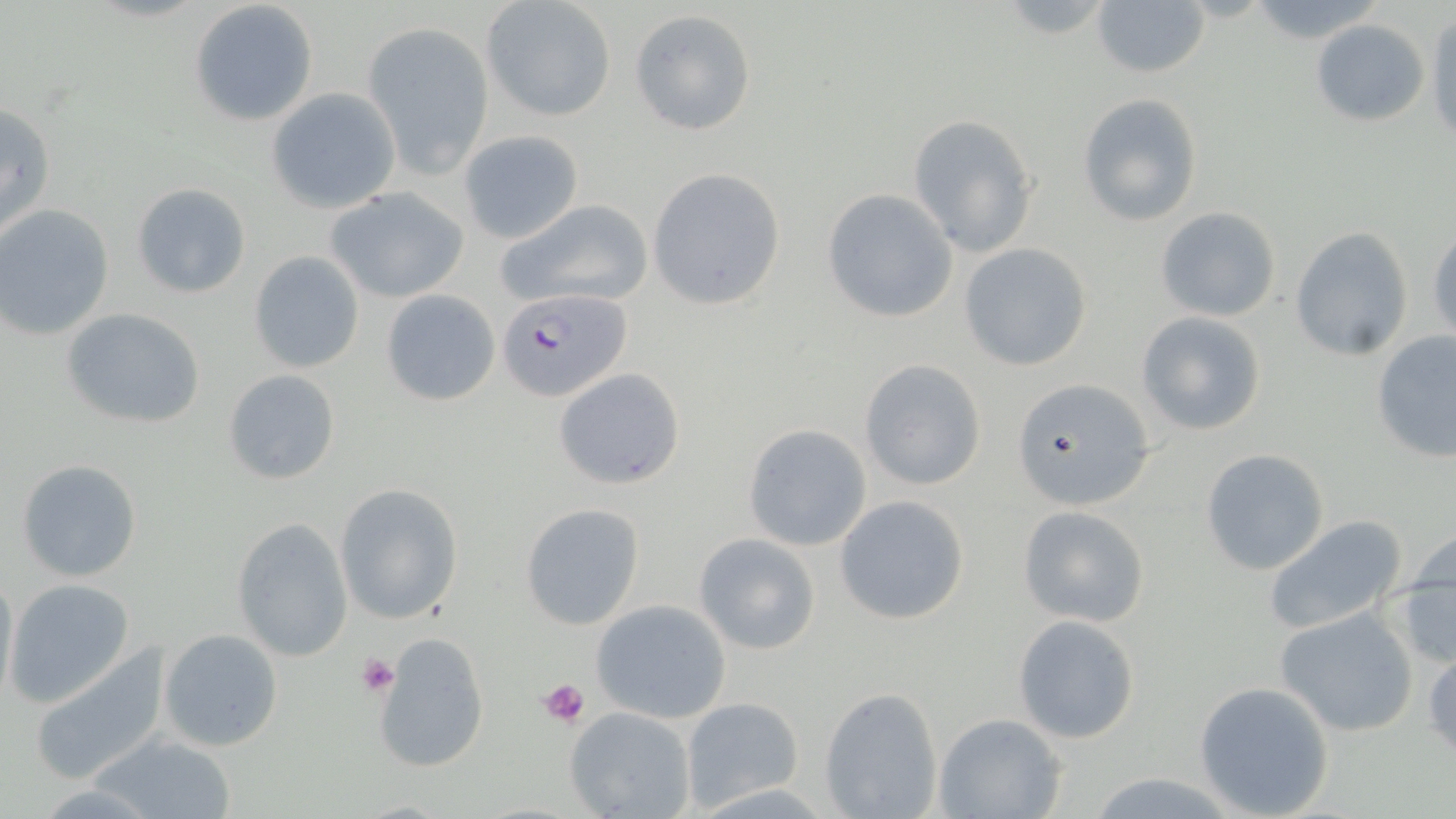

Summary:
  - Coordinate format: approximate bounding boxes as named x1/y1/x2/y2 corners in pixels
  - Platelet locations: (x1=356, y1=654, x2=400, y2=696), (x1=538, y1=676, x2=592, y2=728)
  - Plasmodium falciparum-infected red blood cell locations: (x1=498, y1=289, x2=631, y2=402)
  - Uninfected red blood cell locations: (x1=482, y1=0, x2=616, y2=121), (x1=190, y1=1, x2=317, y2=125), (x1=1092, y1=3, x2=1210, y2=79), (x1=629, y1=9, x2=757, y2=135), (x1=1425, y1=14, x2=1455, y2=150), (x1=1311, y1=18, x2=1429, y2=126), (x1=361, y1=21, x2=494, y2=175), (x1=267, y1=88, x2=401, y2=212), (x1=1077, y1=93, x2=1203, y2=225), (x1=1, y1=99, x2=56, y2=239), (x1=907, y1=114, x2=1039, y2=258), (x1=459, y1=129, x2=584, y2=243), (x1=647, y1=167, x2=786, y2=311), (x1=132, y1=182, x2=249, y2=298), (x1=324, y1=187, x2=469, y2=304), (x1=822, y1=188, x2=958, y2=322), (x1=497, y1=199, x2=654, y2=311), (x1=0, y1=203, x2=115, y2=340), (x1=1156, y1=206, x2=1280, y2=321), (x1=1427, y1=225, x2=1456, y2=343), (x1=1289, y1=226, x2=1414, y2=360), (x1=959, y1=243, x2=1092, y2=371), (x1=249, y1=250, x2=366, y2=372), (x1=379, y1=289, x2=501, y2=407), (x1=61, y1=307, x2=205, y2=428), (x1=1135, y1=310, x2=1268, y2=436), (x1=1371, y1=330, x2=1456, y2=464), (x1=860, y1=359, x2=987, y2=490), (x1=553, y1=367, x2=685, y2=490), (x1=222, y1=370, x2=342, y2=485), (x1=1014, y1=379, x2=1155, y2=509), (x1=742, y1=423, x2=873, y2=552), (x1=1199, y1=448, x2=1329, y2=576), (x1=15, y1=458, x2=143, y2=583), (x1=334, y1=484, x2=464, y2=625), (x1=834, y1=495, x2=970, y2=625), (x1=520, y1=502, x2=646, y2=628), (x1=1017, y1=505, x2=1149, y2=627), (x1=1261, y1=514, x2=1408, y2=637), (x1=230, y1=518, x2=352, y2=661), (x1=693, y1=532, x2=821, y2=654), (x1=1393, y1=539, x2=1456, y2=668), (x1=0, y1=568, x2=19, y2=706), (x1=4, y1=580, x2=134, y2=707), (x1=592, y1=600, x2=731, y2=722), (x1=1275, y1=607, x2=1421, y2=737), (x1=1014, y1=615, x2=1140, y2=744), (x1=159, y1=628, x2=284, y2=753), (x1=370, y1=631, x2=491, y2=773), (x1=28, y1=645, x2=172, y2=787), (x1=1426, y1=648, x2=1456, y2=764), (x1=1193, y1=681, x2=1335, y2=818), (x1=819, y1=685, x2=944, y2=818), (x1=680, y1=696, x2=804, y2=810), (x1=565, y1=706, x2=697, y2=819), (x1=936, y1=713, x2=1067, y2=819), (x1=93, y1=733, x2=238, y2=818)
  - Slide-level diagnosis: Plasmodium falciparum
  - Preparation: thin blood smear
  - Stain: May-Grünwald-Giemsa
  - Image size: 1456×819 pixels
  - Field of view: one of a larger specimen
  - Magnification: 1000x
  - Modality: optical microscopy